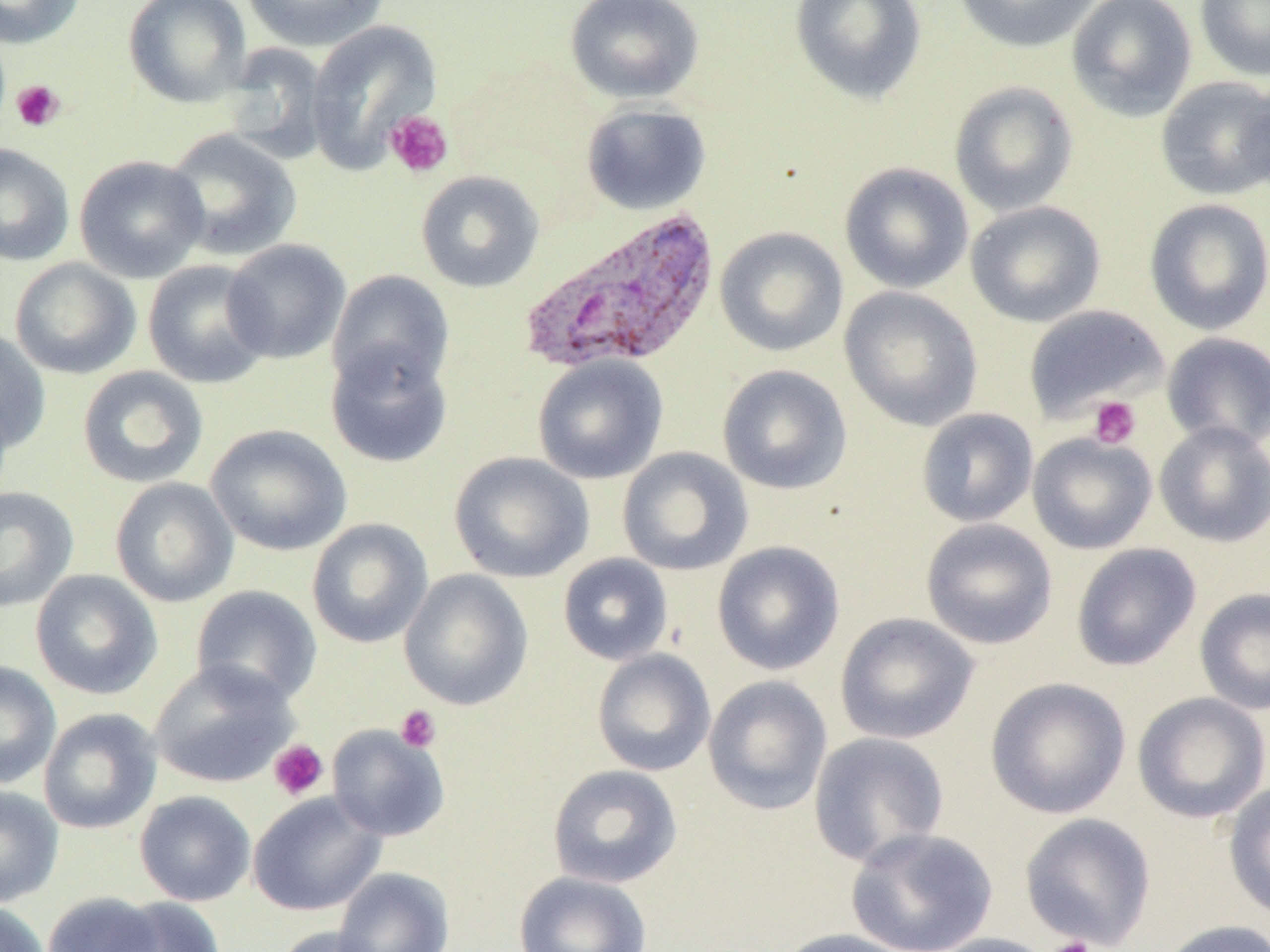

Summary:
  - Coordinate format: approximate bounding boxes as (x1, y1, x2, y2) in pixels
  - Plasmodium vivax-infected red blood cell locations: (520, 205, 721, 377)
  - Uninfected red blood cell locations: (0, 0, 85, 49), (123, 0, 251, 108), (240, 0, 389, 52), (565, 0, 705, 105), (789, 0, 927, 105), (952, 0, 1103, 53), (1067, 0, 1197, 121), (1194, 0, 1270, 81), (306, 21, 443, 171), (221, 43, 334, 163), (1240, 74, 1270, 202), (1155, 76, 1270, 200), (949, 80, 1078, 216), (580, 103, 712, 216), (163, 128, 302, 262), (0, 142, 75, 266), (74, 155, 209, 283), (838, 162, 974, 294), (416, 170, 545, 293), (1143, 198, 1270, 335), (965, 201, 1106, 327), (715, 226, 848, 357), (222, 239, 352, 364), (9, 257, 141, 380), (143, 259, 274, 389), (327, 270, 455, 396), (839, 287, 983, 431), (1023, 304, 1169, 422), (0, 327, 51, 455), (1161, 332, 1270, 451), (325, 341, 453, 469), (532, 355, 668, 484), (717, 364, 853, 495), (77, 366, 209, 489), (916, 407, 1039, 527), (1154, 421, 1270, 547), (206, 424, 352, 556), (1027, 433, 1157, 555), (617, 447, 754, 576), (449, 452, 594, 583), (110, 477, 239, 607), (0, 487, 79, 612), (306, 518, 433, 649), (920, 518, 1058, 650), (712, 541, 845, 676), (1071, 543, 1201, 671), (557, 553, 674, 666), (399, 568, 533, 710), (30, 569, 163, 700), (190, 585, 322, 708), (1194, 586, 1270, 716), (834, 612, 980, 745), (591, 648, 716, 777), (149, 659, 299, 789), (0, 660, 61, 790), (703, 675, 833, 816), (985, 677, 1131, 819), (1132, 691, 1270, 824), (38, 708, 162, 835), (327, 724, 449, 841), (808, 731, 950, 868), (547, 764, 683, 889), (1223, 782, 1270, 922), (0, 784, 64, 908), (134, 790, 256, 906), (248, 792, 386, 916), (1019, 813, 1156, 949), (846, 827, 998, 952), (332, 867, 455, 952), (513, 871, 653, 952), (41, 892, 167, 952), (106, 897, 226, 952), (0, 901, 50, 952), (1156, 919, 1270, 952), (272, 926, 391, 952), (771, 928, 920, 952), (924, 933, 1059, 952)
  - Platelet locations: (11, 79, 65, 132), (385, 110, 453, 179), (1088, 396, 1141, 449), (395, 705, 442, 753), (269, 739, 329, 801), (1047, 936, 1097, 952)
  - Slide-level diagnosis: Plasmodium vivax
  - Image size: 1270×952 pixels
  - Field of view: one of a larger specimen
  - Preparation: thin blood smear
  - Modality: light microscopy
  - Magnification: 1000x